Assess this cell for malaria.
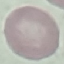
Uninfected.

Summary:
  - Capture: smartphone through the microscope eyepiece
  - Stain: Giemsa
  - Image type: cell patch, automatically extracted from a larger field of view and resized to 64 × 64 pixels
  - Preparation: thin blood film